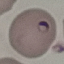

{
  "result": "malaria parasites identified",
  "capture": "smartphone camera at the microscope eyepiece",
  "stain": "Giemsa",
  "preparation": "thin smear",
  "image_type": "automatically extracted cell patch, resized to 64 × 64 pixels"
}